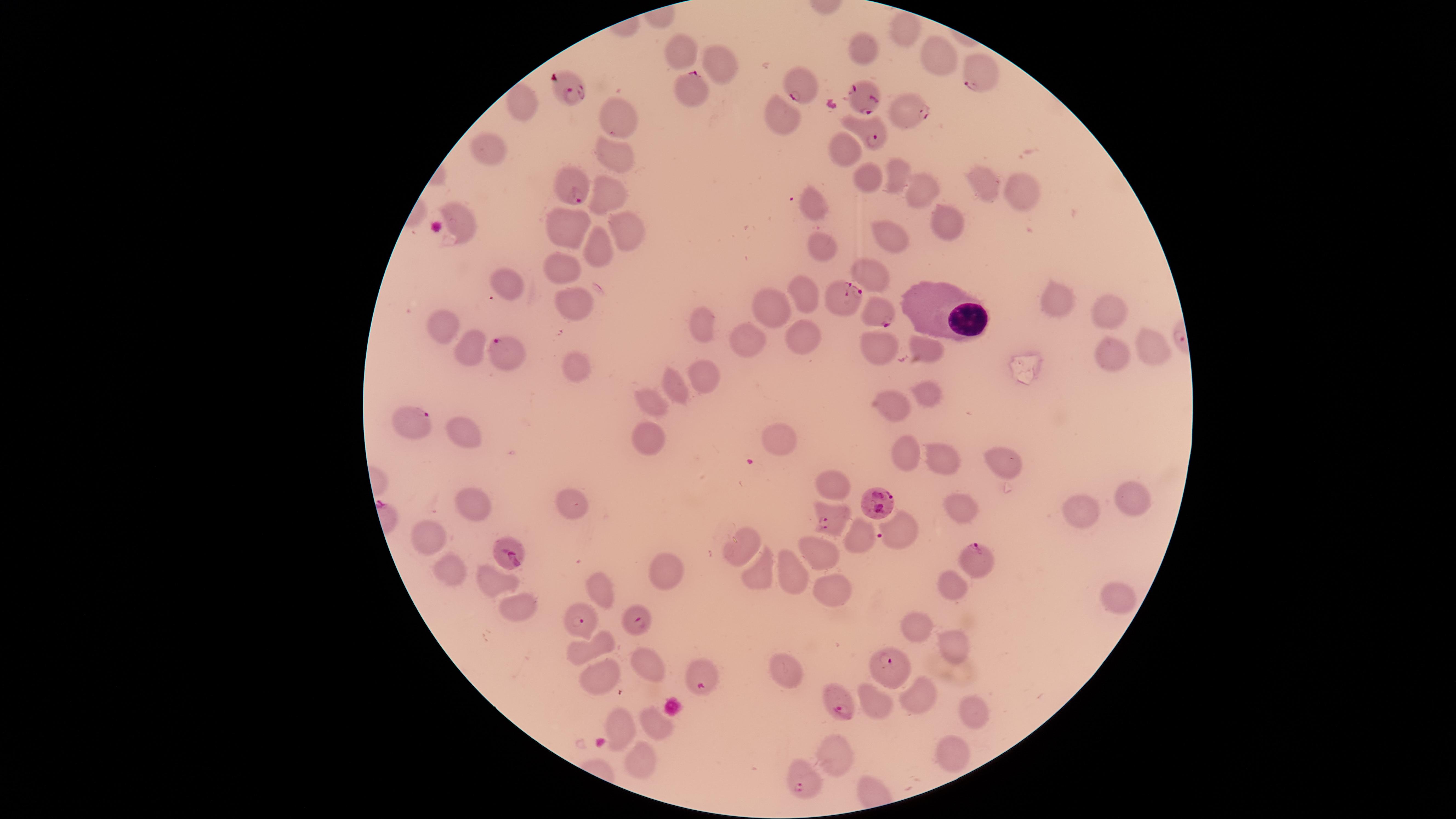
Approximate marker points as {x, y} in pixels. White blood cells: {936, 305}. Parasitized red blood cells: {972, 75}, {802, 85}, {570, 88}, {689, 88}, {868, 102}, {903, 109}, {869, 131}, {565, 184}, {846, 298}, {880, 309}, {509, 350}, {876, 501}, {828, 519}, {512, 552}, {980, 559}, {582, 622}, {635, 623}, {895, 664}, {706, 677}, {837, 698}, {801, 782}. Uninfected red blood cells: {914, 26}, {862, 48}, {684, 53}, {937, 58}, {725, 63}, {523, 103}, {621, 115}, {786, 119}, {842, 147}, {615, 155}, {486, 160}, {895, 175}, {863, 177}, {981, 180}, {1021, 181}, {918, 186}, {609, 198}, {813, 204}, {570, 220}, {945, 221}, {461, 226}, {625, 228}, {894, 232}, {823, 240}, {596, 250}, {561, 261}, {871, 271}, {506, 279}, {809, 291}, {1056, 302}, {568, 305}, {773, 309}, {1102, 313}, {444, 326}, {703, 327}, {748, 335}, {807, 335}, {1154, 342}, {881, 343}, {475, 344}, {926, 348}, {1109, 355}, {571, 358}, {709, 378}, {675, 383}, {926, 386}, {656, 397}, {897, 400}, {415, 419}, {459, 428}, {646, 435}, {777, 439}, {904, 444}, {1006, 455}, {938, 459}, {833, 478}, {1131, 496}, {575, 502}, {473, 503}, {958, 504}, {1079, 512}, {859, 528}, {895, 530}, {427, 539}, {739, 544}, {813, 553}, {754, 568}, {450, 569}, {790, 570}, {662, 572}, {494, 577}, {952, 579}, {602, 588}, {1112, 596}, {828, 597}, {514, 605}, {920, 623}, {954, 644}, {580, 651}, {647, 662}, {787, 674}, {604, 680}, {919, 687}, {876, 704}, {970, 712}, {652, 717}, {622, 722}, {943, 750}, {837, 752}, {640, 757}. Species: Plasmodium falciparum. Circular visible region. Presence: malaria parasites detected. Image is 1456×819 pixels. Giemsa stain. Smartphone photograph through the microscope eyepiece. Thin smear of blood. One field of view of the specimen.